Give the extent of all uninfected red blood cells.
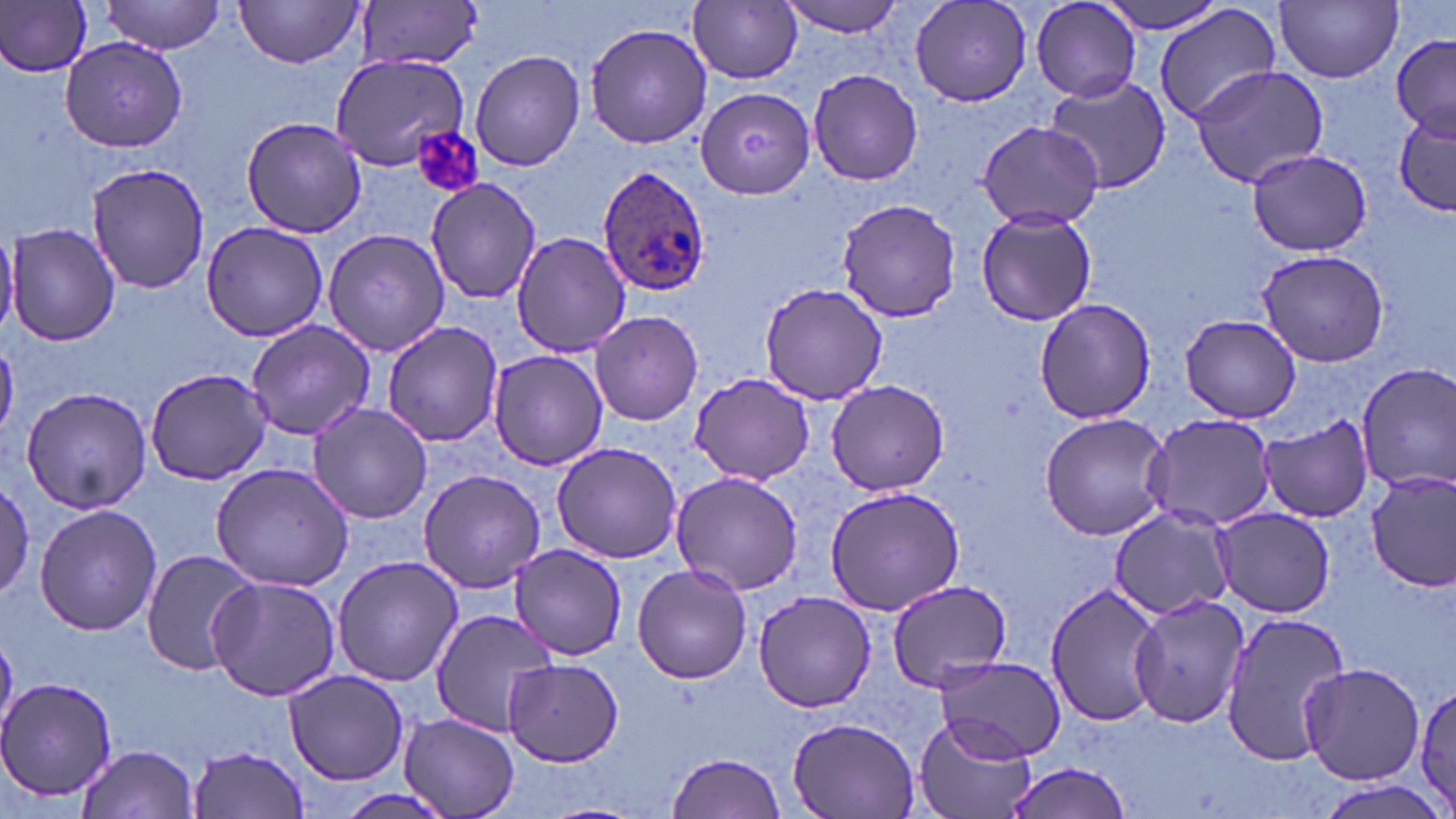

Approximate bounding boxes as named x1/y1/x2/y2 corners in pixels.
Uninfected red blood cells: (x1=99, y1=0, x2=226, y2=54), (x1=777, y1=0, x2=912, y2=38), (x1=1031, y1=0, x2=1142, y2=101), (x1=1095, y1=0, x2=1229, y2=34), (x1=234, y1=1, x2=367, y2=69), (x1=910, y1=1, x2=1033, y2=107), (x1=1276, y1=1, x2=1402, y2=84), (x1=0, y1=2, x2=93, y2=78), (x1=357, y1=2, x2=479, y2=71), (x1=690, y1=2, x2=803, y2=84), (x1=1156, y1=3, x2=1281, y2=127), (x1=585, y1=22, x2=712, y2=151), (x1=1391, y1=33, x2=1455, y2=140), (x1=59, y1=35, x2=189, y2=152), (x1=469, y1=49, x2=587, y2=172), (x1=327, y1=54, x2=471, y2=171), (x1=1189, y1=65, x2=1330, y2=188), (x1=808, y1=69, x2=923, y2=187), (x1=1046, y1=74, x2=1171, y2=193), (x1=695, y1=86, x2=814, y2=200), (x1=1394, y1=109, x2=1454, y2=216), (x1=241, y1=116, x2=368, y2=237), (x1=978, y1=120, x2=1105, y2=230), (x1=1245, y1=150, x2=1377, y2=256), (x1=84, y1=162, x2=212, y2=295), (x1=425, y1=177, x2=541, y2=304), (x1=837, y1=198, x2=960, y2=322), (x1=977, y1=208, x2=1097, y2=325), (x1=199, y1=221, x2=330, y2=343), (x1=6, y1=223, x2=119, y2=348), (x1=0, y1=227, x2=18, y2=338), (x1=322, y1=227, x2=452, y2=357), (x1=510, y1=230, x2=631, y2=356), (x1=1254, y1=247, x2=1392, y2=369), (x1=758, y1=282, x2=891, y2=405), (x1=1033, y1=299, x2=1159, y2=425), (x1=589, y1=310, x2=703, y2=426), (x1=1179, y1=313, x2=1301, y2=422), (x1=246, y1=319, x2=377, y2=440), (x1=382, y1=320, x2=504, y2=446), (x1=487, y1=351, x2=608, y2=471), (x1=1356, y1=365, x2=1456, y2=490), (x1=144, y1=366, x2=272, y2=486), (x1=688, y1=372, x2=815, y2=486), (x1=825, y1=379, x2=949, y2=496), (x1=20, y1=386, x2=153, y2=514), (x1=307, y1=401, x2=435, y2=525), (x1=1038, y1=412, x2=1174, y2=539), (x1=1143, y1=413, x2=1277, y2=531), (x1=1258, y1=416, x2=1374, y2=523), (x1=551, y1=441, x2=684, y2=564), (x1=210, y1=461, x2=356, y2=590), (x1=418, y1=469, x2=548, y2=594), (x1=1365, y1=470, x2=1455, y2=594), (x1=670, y1=471, x2=807, y2=596), (x1=0, y1=481, x2=35, y2=601), (x1=825, y1=485, x2=965, y2=615), (x1=34, y1=502, x2=160, y2=636), (x1=1107, y1=504, x2=1240, y2=621), (x1=1213, y1=507, x2=1337, y2=619), (x1=508, y1=544, x2=631, y2=659), (x1=140, y1=549, x2=259, y2=677), (x1=330, y1=554, x2=465, y2=686), (x1=632, y1=563, x2=752, y2=683), (x1=207, y1=574, x2=340, y2=701), (x1=883, y1=580, x2=1016, y2=694), (x1=1045, y1=581, x2=1168, y2=729), (x1=751, y1=589, x2=876, y2=714), (x1=1128, y1=592, x2=1250, y2=729), (x1=428, y1=609, x2=557, y2=737), (x1=1218, y1=611, x2=1351, y2=767), (x1=930, y1=655, x2=1066, y2=763), (x1=503, y1=658, x2=625, y2=767), (x1=1300, y1=662, x2=1424, y2=785), (x1=284, y1=669, x2=409, y2=785), (x1=1, y1=676, x2=117, y2=805), (x1=1411, y1=681, x2=1456, y2=813), (x1=399, y1=714, x2=519, y2=818), (x1=787, y1=714, x2=921, y2=818), (x1=916, y1=714, x2=1037, y2=819), (x1=79, y1=744, x2=199, y2=819), (x1=191, y1=745, x2=310, y2=818), (x1=667, y1=752, x2=787, y2=819), (x1=1003, y1=757, x2=1135, y2=819).

Platelet locations: (x1=411, y1=128, x2=481, y2=199). Plasmodium ovale-infected red blood cell locations: (x1=598, y1=166, x2=714, y2=295). Slide-level diagnosis: Plasmodium ovale. May-Grünwald-Giemsa stain. Thin blood smear. 1000x magnification. One field of a larger specimen. Light microscopy. Image is 1456×819 pixels.